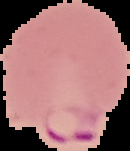

Summary:
  - Image type: segmented cell region on a black background
  - Result: Plasmodium parasites identified
  - Preparation: thin blood film
  - Image size: 130×151 pixels